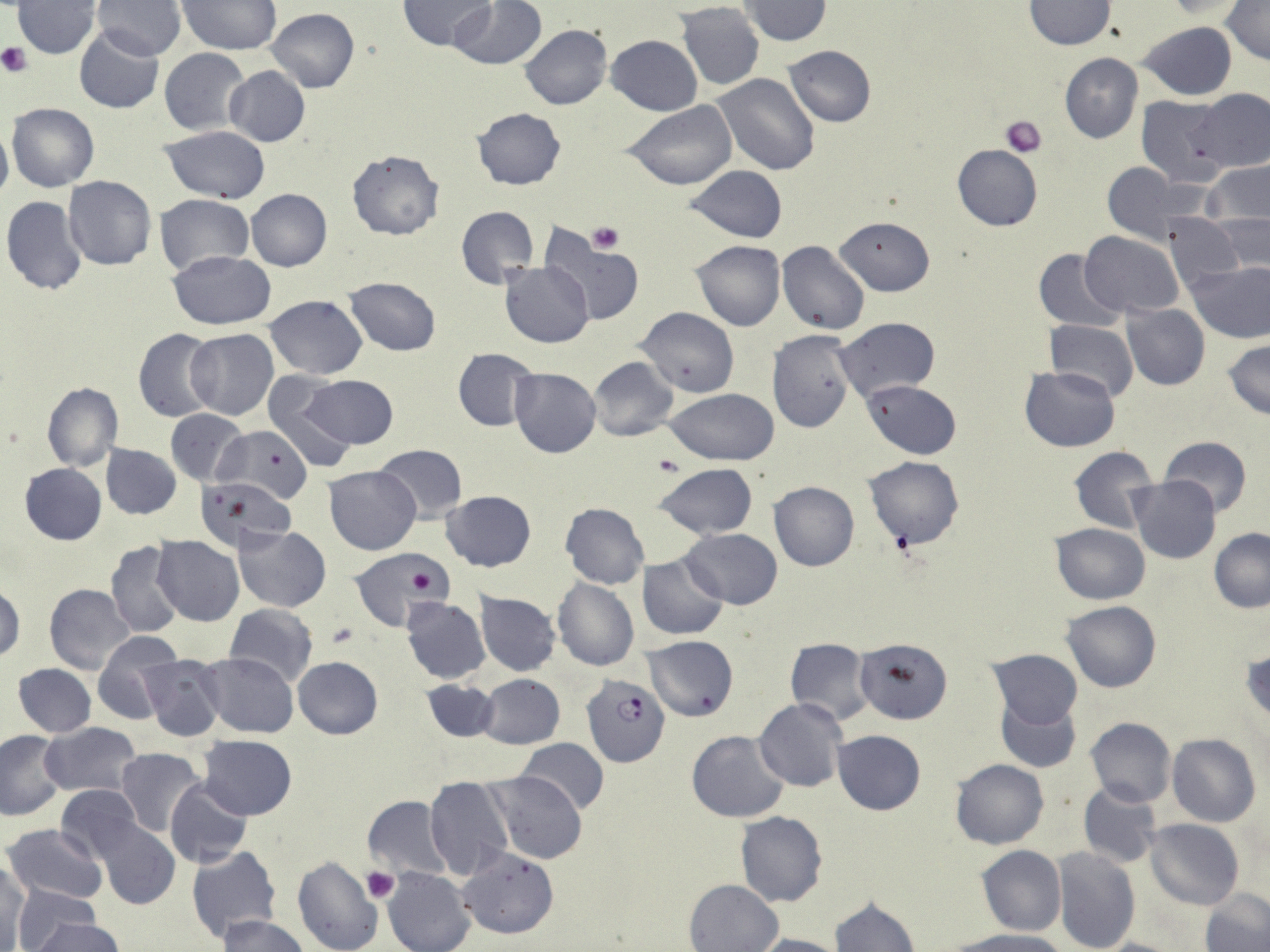
slide-level diagnosis = Plasmodium falciparum
magnification = 1000x
image size = 1270×952 pixels
platelet locations = approximate bounding boxes as (x1,y1)-(x2,y2) corner pairs in pixels: (0,42)-(32,77), (1001,115)-(1047,156), (587,222)-(623,254), (654,453)-(685,477), (328,623)-(360,649), (361,867)-(397,903)
preparation = thin blood smear
Plasmodium falciparum-infected red blood cell locations = approximate bounding boxes as (x1,y1)-(x2,y2) corner pairs in pixels: (582,672)-(670,767)
stain = May-Grünwald-Giemsa
field of view = one of a larger specimen
uninfected red blood cell locations = approximate bounding boxes as (x1,y1)-(x2,y2) corner pairs in pixels: (92,0)-(186,60), (178,0)-(282,54), (398,0)-(494,51), (448,0)-(547,70), (738,0)-(832,45), (1023,0)-(1115,49), (1163,1)-(1248,20), (13,2)-(101,58), (1221,2)-(1270,66), (676,3)-(764,90), (267,8)-(359,92), (1137,21)-(1238,100), (520,24)-(612,109), (74,27)-(165,113), (606,35)-(702,115), (784,45)-(877,127), (160,48)-(251,135), (1060,53)-(1142,144), (224,66)-(310,147), (712,72)-(820,176), (1194,89)-(1270,171), (1136,95)-(1231,184), (624,102)-(736,190), (6,103)-(99,192), (471,107)-(567,190), (0,122)-(12,205), (160,125)-(271,204), (951,144)-(1042,230), (347,149)-(445,240), (1203,159)-(1270,230), (1101,163)-(1198,245), (684,165)-(788,243), (63,176)-(157,270), (246,189)-(331,271), (154,194)-(253,276), (2,196)-(90,296), (455,206)-(538,290), (1163,214)-(1246,293), (1209,214)-(1270,274), (834,216)-(935,296), (540,228)-(646,327), (1080,231)-(1184,317), (691,239)-(786,331), (777,241)-(870,335), (168,249)-(277,329), (1035,249)-(1126,332), (501,262)-(593,346), (1186,262)-(1270,342), (344,276)-(441,354), (264,296)-(368,379), (1121,303)-(1211,390), (635,307)-(738,397), (834,317)-(940,400), (1045,320)-(1139,403), (134,328)-(219,423), (186,328)-(278,419), (767,329)-(856,432), (1223,340)-(1270,419), (450,347)-(539,432), (588,356)-(677,440), (1019,366)-(1119,451), (509,367)-(602,457), (261,374)-(357,471), (299,375)-(399,449), (864,378)-(962,457), (41,382)-(123,470), (665,389)-(778,464), (662,391)-(766,540), (166,408)-(247,485), (219,423)-(313,504), (1158,435)-(1254,515), (101,444)-(181,518), (374,444)-(468,521), (1069,446)-(1159,533), (864,456)-(965,551), (19,463)-(107,545), (653,463)-(757,540), (324,465)-(420,555), (1128,477)-(1221,564), (205,480)-(303,578), (768,481)-(859,571), (442,490)-(536,571), (561,502)-(649,589), (1050,523)-(1151,605), (234,525)-(330,612), (681,527)-(783,609), (1209,528)-(1270,613), (152,535)-(244,626), (105,541)-(183,638), (351,548)-(452,631), (637,555)-(729,641), (552,579)-(640,670), (0,581)-(24,664), (44,584)-(137,676), (475,592)-(561,674), (401,597)-(490,683), (1061,601)-(1161,692), (225,604)-(317,689), (91,632)-(181,724), (643,636)-(739,721), (785,639)-(873,725), (856,639)-(953,723), (987,649)-(1082,729), (197,653)-(299,736), (140,656)-(225,740), (293,656)-(383,739), (11,664)-(96,738), (477,674)-(565,749), (421,679)-(501,742), (995,694)-(1080,772), (754,698)-(847,793), (1085,717)-(1176,807), (41,723)-(143,796), (832,729)-(925,816), (0,730)-(66,819), (687,730)-(790,821), (1168,734)-(1261,827), (199,735)-(297,819), (517,739)-(609,816), (115,748)-(205,836), (949,759)-(1049,850), (483,771)-(586,864), (166,777)-(253,869), (424,777)-(514,880), (1077,781)-(1163,869), (56,785)-(145,863), (362,797)-(452,880), (735,811)-(827,906), (1144,819)-(1245,910), (3,823)-(108,905), (95,823)-(180,910), (191,844)-(280,942), (976,844)-(1066,936), (457,847)-(559,939), (1052,848)-(1141,952), (291,856)-(384,952), (0,857)-(28,949), (383,868)-(476,952), (684,878)-(783,951), (12,884)-(100,951), (1201,890)-(1270,952), (830,895)-(920,952), (221,915)-(307,951), (23,917)-(122,952), (951,929)-(1069,952), (751,934)-(844,952), (1090,938)-(1182,952)
modality = optical microscopy